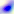

Summary:
  - Magnification: 400x
  - Modality: photomicrograph
  - Identification: Toxoplasma gondii